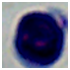
modality = photomicrograph
identification = white blood cell
magnification = 1000x